Outline each Plasmodium falciparum-infected red blood cell.
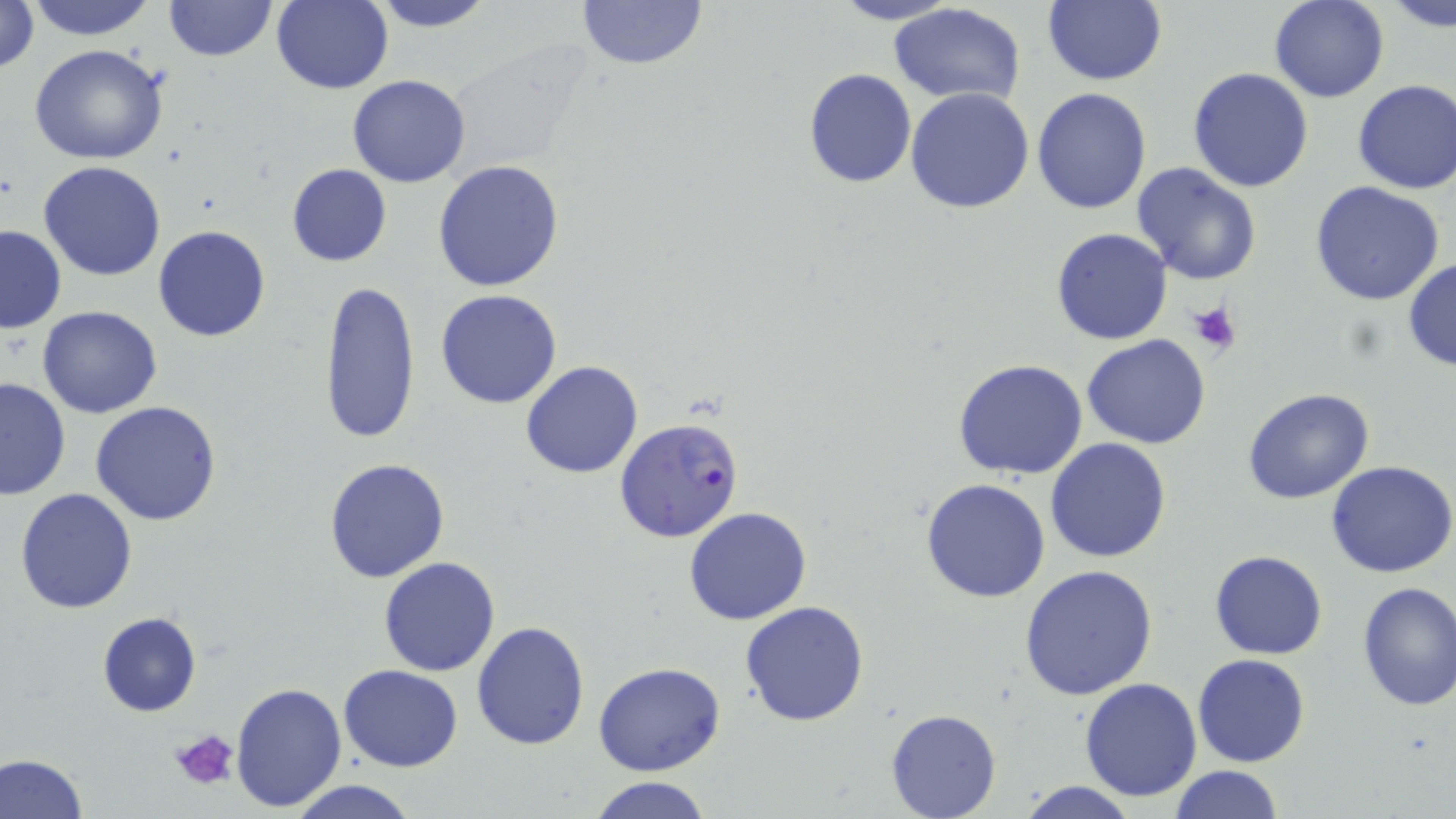

Approximate bounding boxes as (x1, y1, x2, y2) in pixels.
Plasmodium falciparum-infected red blood cells: (615, 416, 743, 541).

slide-level diagnosis = Plasmodium falciparum
modality = optical microscopy
stain = May-Grünwald-Giemsa
magnification = 1000x
preparation = thin blood film
field of view = single
uninfected red blood cell locations = approximate bounding boxes as (x1, y1, x2, y2) in pixels: (25, 0, 158, 41), (163, 0, 276, 61), (365, 0, 499, 31), (575, 0, 709, 72), (827, 0, 965, 26), (1041, 0, 1167, 86), (1269, 0, 1390, 103), (1, 1, 40, 75), (272, 1, 393, 95), (1384, 1, 1455, 31), (887, 4, 1026, 106), (28, 44, 170, 166), (802, 67, 918, 188), (1187, 67, 1314, 192), (347, 75, 472, 188), (1352, 78, 1456, 195), (1031, 87, 1152, 214), (905, 88, 1034, 214), (432, 159, 565, 292), (38, 161, 167, 281), (1131, 161, 1261, 285), (286, 163, 393, 267), (1309, 180, 1445, 304), (0, 225, 67, 335), (153, 225, 272, 342), (1051, 228, 1174, 346), (1402, 259, 1456, 371), (319, 280, 422, 448), (435, 290, 563, 409), (37, 305, 163, 418), (1082, 333, 1211, 450), (953, 358, 1089, 480), (520, 360, 643, 478), (0, 377, 71, 502), (1242, 386, 1376, 504), (90, 401, 223, 525), (1046, 438, 1172, 563), (323, 457, 450, 583), (1327, 461, 1456, 579), (921, 478, 1052, 603), (14, 486, 139, 613), (684, 506, 813, 625), (1210, 551, 1328, 659), (379, 556, 501, 676), (1018, 564, 1159, 703), (1355, 581, 1456, 710), (739, 600, 869, 728), (97, 610, 201, 716), (471, 621, 592, 752), (1193, 653, 1310, 767), (593, 660, 726, 776), (337, 663, 464, 772), (1079, 678, 1203, 802), (229, 680, 347, 813), (885, 709, 1000, 819), (0, 752, 87, 819), (1168, 765, 1283, 819), (586, 776, 715, 819), (284, 779, 421, 819), (1015, 779, 1139, 818)
image size = 1456×819 pixels
platelet locations = approximate bounding boxes as (x1, y1, x2, y2) in pixels: (1185, 300, 1241, 356), (168, 727, 242, 793)